State which cell type is depicted.
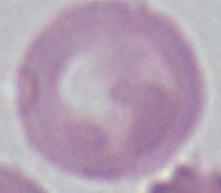

An erythrocyte.

Summary:
  - Modality: micrograph
  - Magnification: 1000x